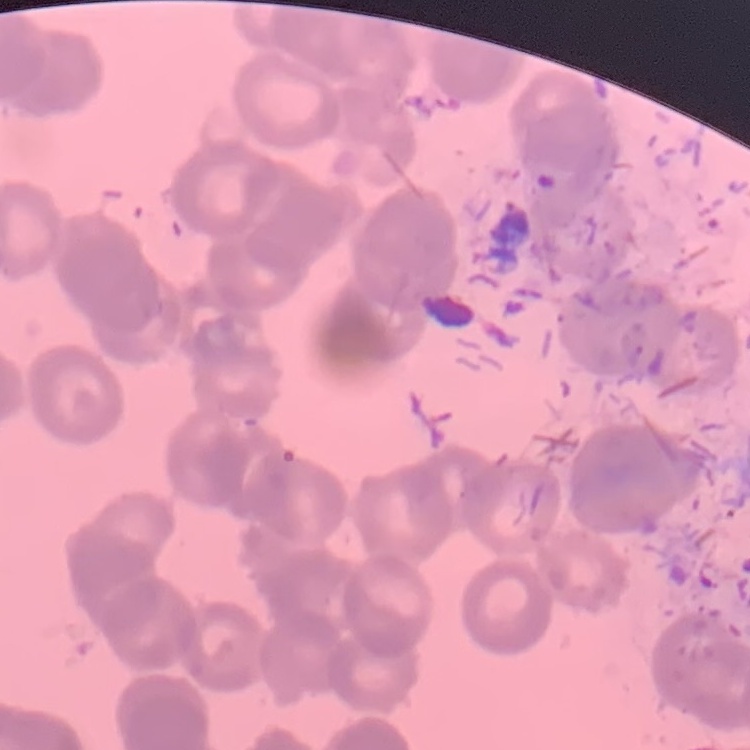 The erythrocytes show rouleaux formation. Thin peripheral smear. Square crop of a larger photomicrograph. Field's or Giemsa stain.